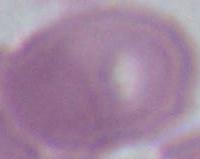

magnification = 1000x
modality = micrograph
identification = erythrocyte